State the preparation type.
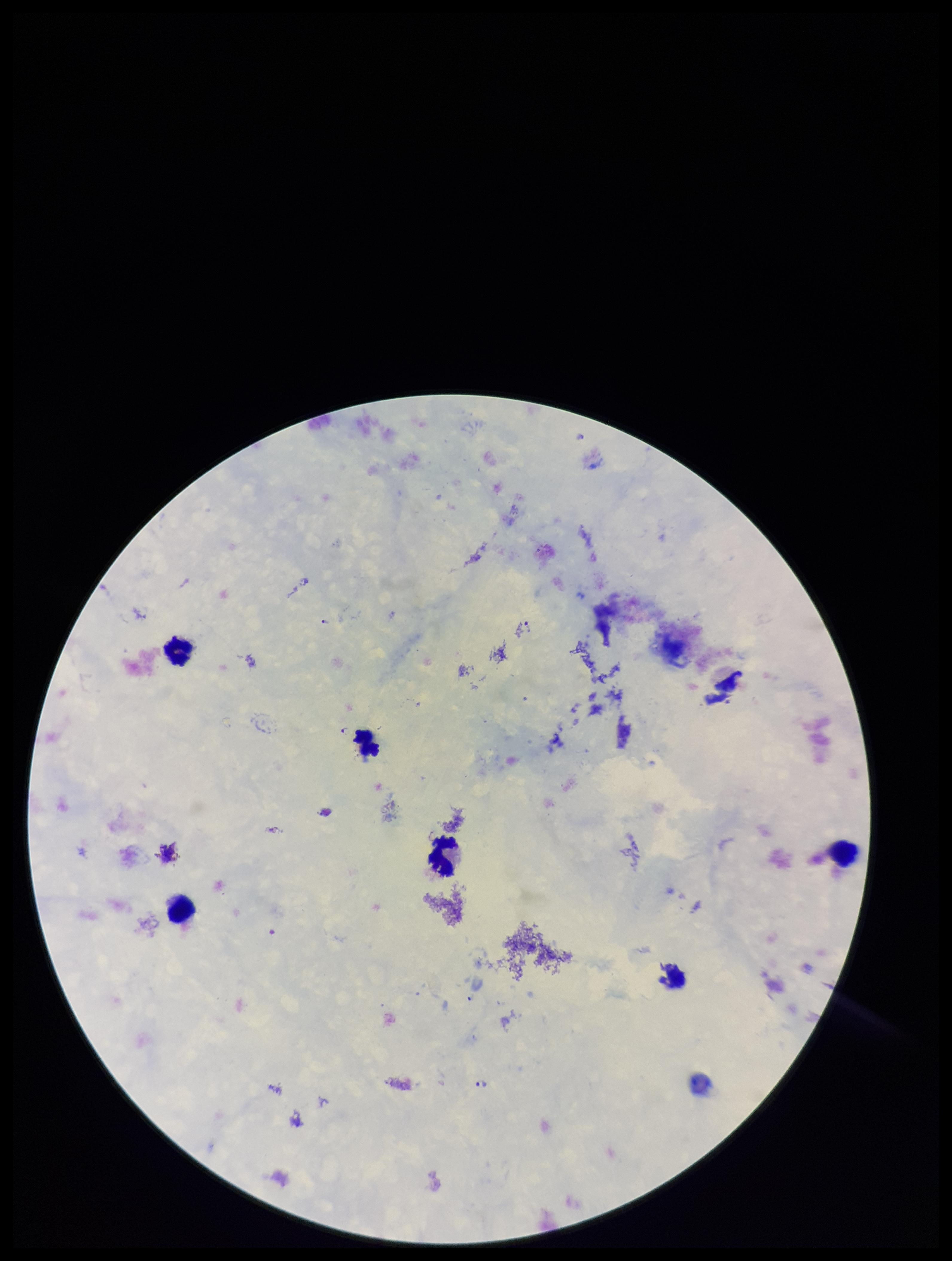

It is a thick blood smear.

Summary:
  - Capture: smartphone photograph through the microscope eyepiece
  - Field of view: one from this slide
  - Stain: Giemsa
  - Leukocyte count: 6
  - Species reported for this patient: Plasmodium falciparum
  - Patient malaria status: infected
  - Plasmodium parasites: identified
  - Image size: 952×1261 pixels
  - Parasite count: 7